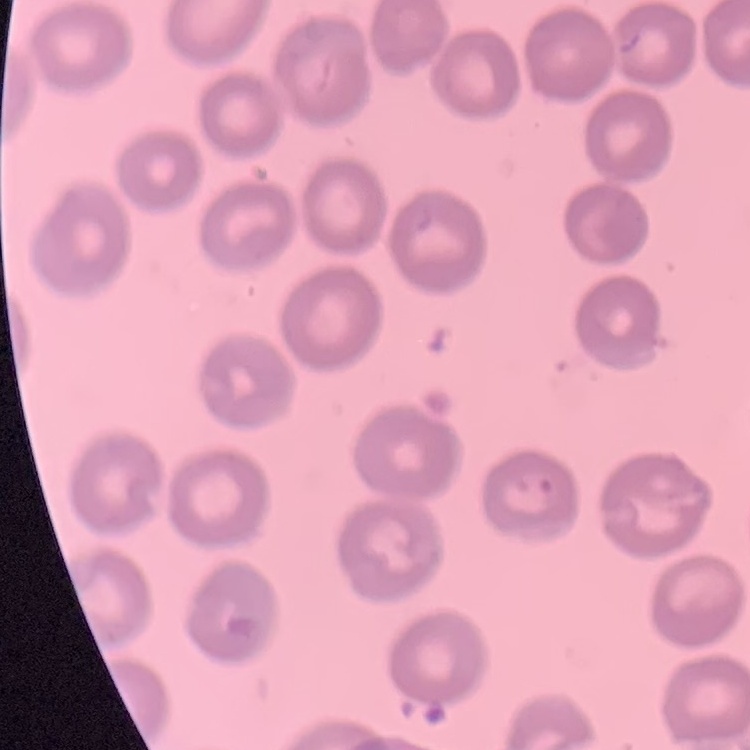

{
  "red_blood_cell_morphology": "no rouleaux formation",
  "stain": "Field's or Giemsa",
  "image_type": "square crop of a larger photomicrograph",
  "preparation": "thin blood smear"
}